Report the malaria status.
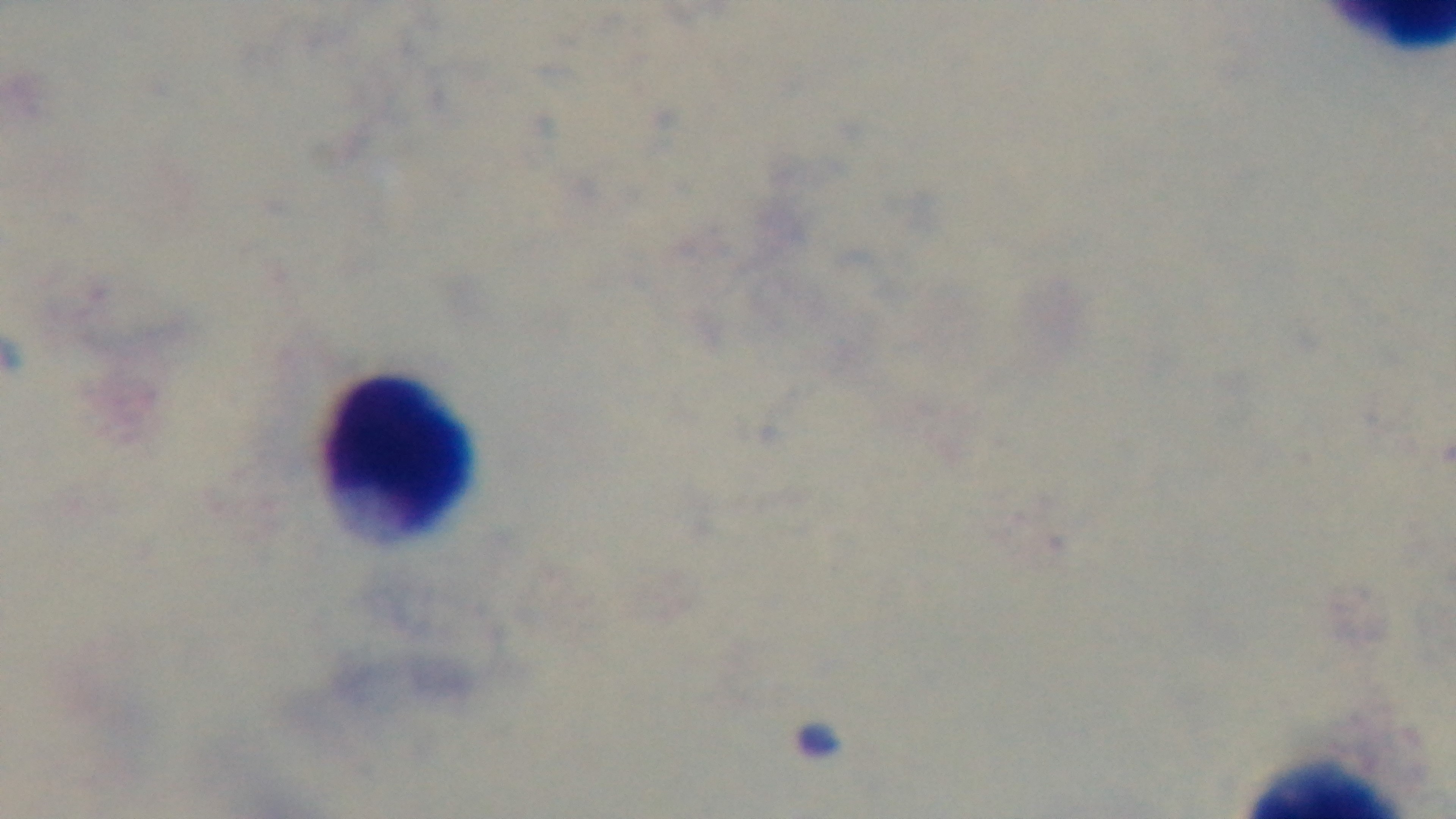

Negative.

Summary:
  - Field of view: one from the slide
  - Modality: light microscopy
  - Stain: Giemsa
  - Capture: mounted 4K digital camera
  - Objective: 100x oil immersion
  - Preparation: thick